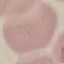
Malaria status: uninfected. Photographed with a smartphone camera at the microscope eyepiece. Giemsa-stained preparation. Thin blood smear. Automatically extracted cell patch, resized to 64 × 64 pixels.